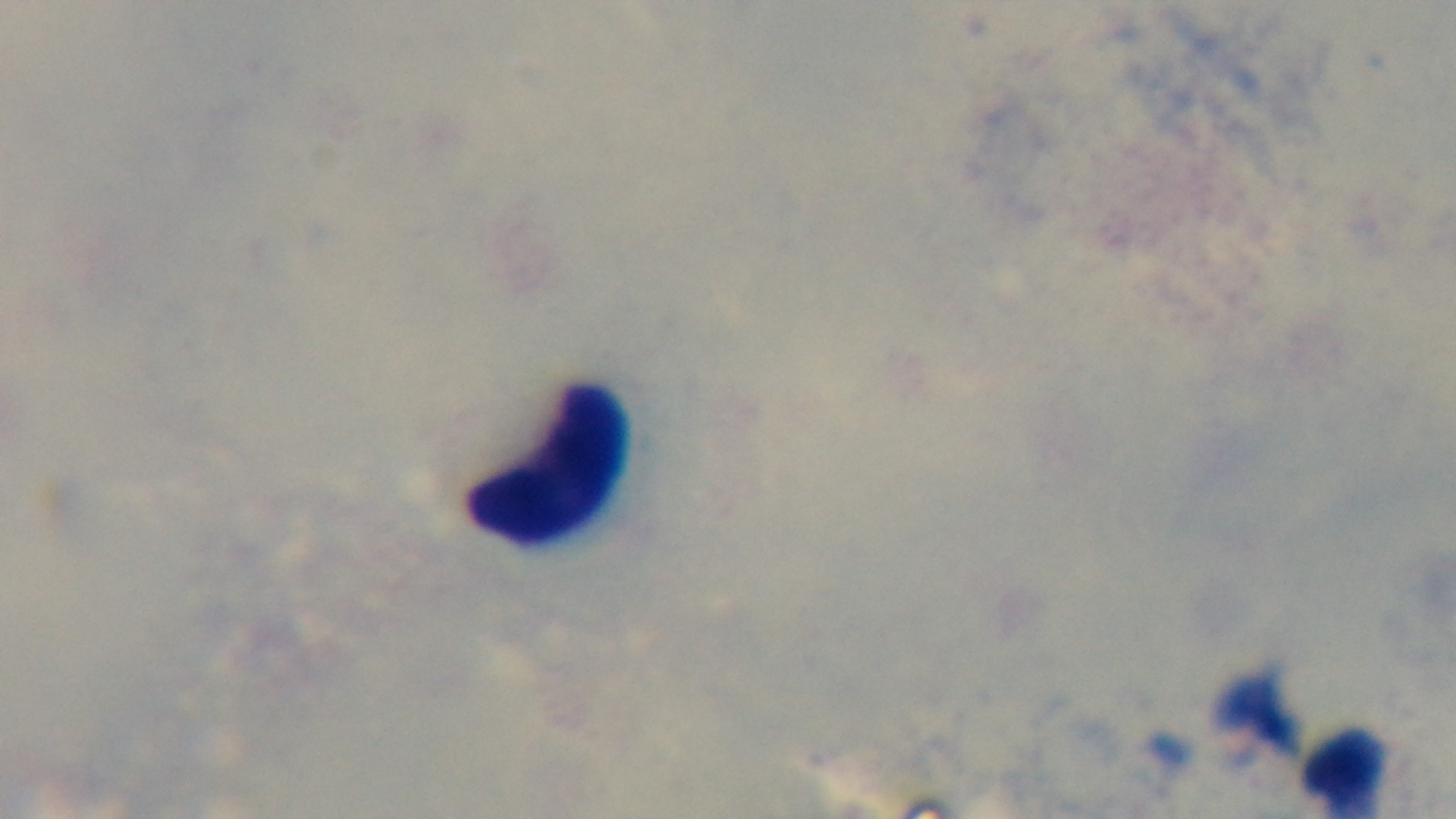 Oil-immersion objective, 100x. One field from the slide. Malaria status: negative. Giemsa-stained. Mounted 4K digital camera. Preparation: thick. Light microscopy.